Report the malaria status of this cell.
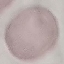
Uninfected.

preparation = thin blood film
stain = Giemsa
image type = cell patch, automatically extracted from a larger field of view and resized to 64 × 64 pixels
capture = smartphone camera at the microscope eyepiece